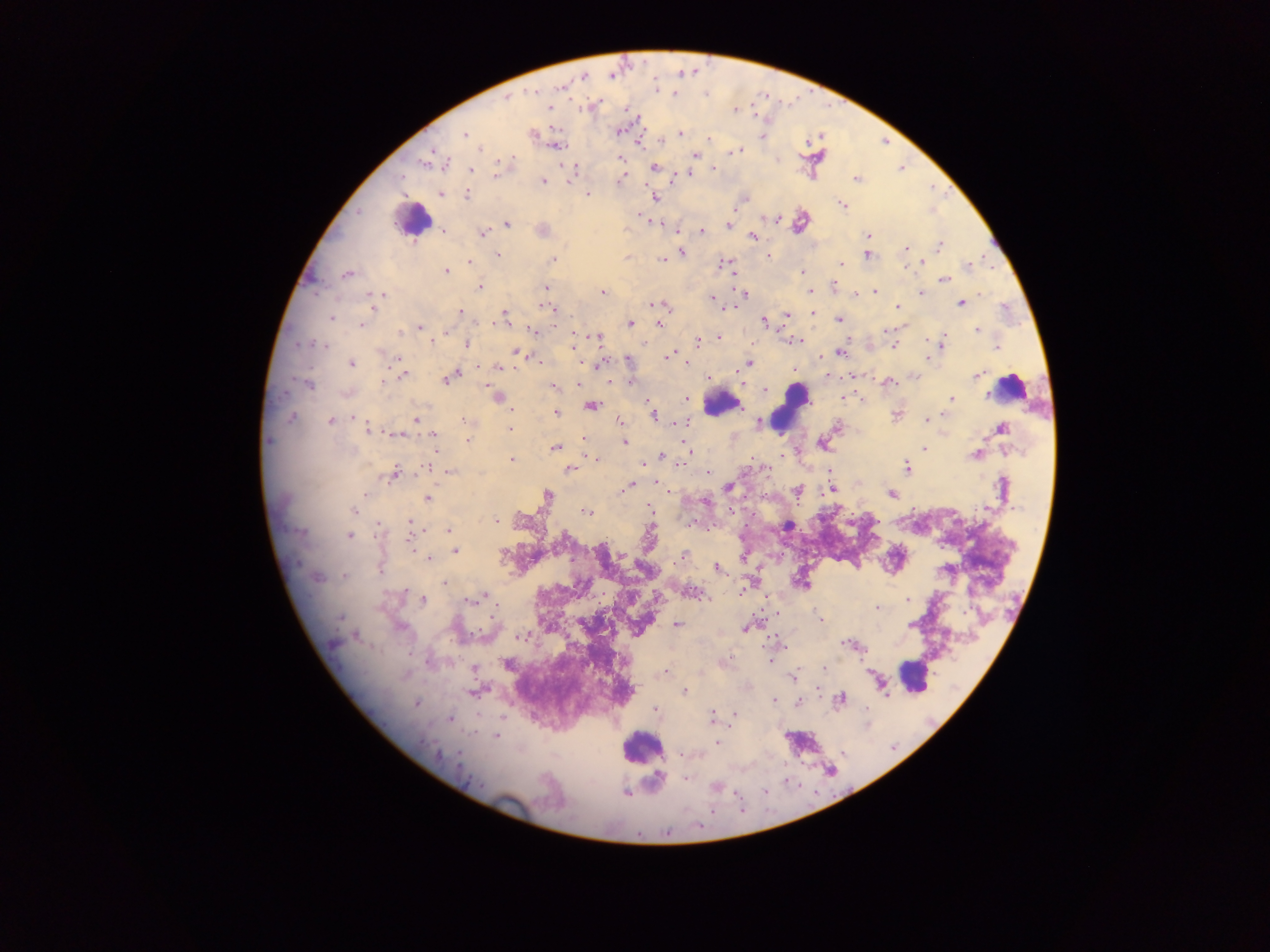
Approximate centers as x y in pixels.
Summary:
  - Plasmodium parasite locations: 561 87; 533 93; 507 98; 548 108; 735 110; 618 131; 680 133; 465 135; 532 135; 763 136; 709 139; 556 145; 479 148; 739 149; 694 155; 621 158; 425 162; 445 164; 655 167; 713 168; 471 169; 573 170; 497 173; 688 174; 857 179; 619 180; 543 181; 441 194; 588 194; 467 195; 655 197; 744 199; 842 204; 508 224; 728 224; 542 230; 702 230; 444 231; 482 233; 869 236; 753 237; 940 246; 906 248; 682 252; 498 255; 868 255; 768 256; 661 259; 553 260; 470 262; 725 263; 923 263; 841 264; 967 266; 803 271; 446 272; 347 275; 943 279; 479 286; 834 287; 546 288; 810 291; 876 291; 603 292; 920 292; 382 294; 743 294; 857 295; 370 296; 712 300; 372 301; 961 303; 658 304; 897 306; 549 308; 461 311; 504 313; 812 313; 787 315; 331 318; 839 319; 504 321; 764 322; 630 323; 361 324; 658 324; 420 327; 978 330; 533 331; 886 331; 400 332; 596 338; 718 338; 431 341; 698 341; 797 341; 941 343; 311 344; 467 344; 324 346; 892 346; 997 348; 518 353; 840 353; 668 356; 927 358; 399 360; 628 360; 685 362; 748 363; 351 364; 497 367; 454 374; 402 375; 827 375; 977 376; 450 378; 385 381; 631 382; 888 382; 307 383; 577 383; 554 388; 766 390; 495 396; 686 397; 844 398; 952 398; 592 406; 555 413; 895 414; 654 415; 291 418; 354 418; 415 420; 462 420; 620 420; 926 420; 330 421; 683 423; 758 424; 369 429; 1001 429; 510 430; 397 434; 433 435; 583 439; 468 440; 268 441; 624 442; 822 444; 555 448; 924 448; 689 452; 661 455; 974 455; 594 459; 511 460; 643 463; 429 467; 906 468; 570 470; 450 472; 393 474; 708 474; 657 482; 628 487; 728 487; 797 490; 832 490; 364 495; 548 495; 892 495; 428 498; 353 510; 586 513; 496 521; 409 523; 789 526; 378 527; 448 530; 350 536; 410 541; 455 550; 684 555; 429 558; 718 569; 380 571; 343 576; 318 578; 443 583; 691 592; 486 597; 479 598; 423 600; 908 600; 470 601; 877 608; 341 618; 820 619; 677 624; 910 625; 401 627; 747 627; 521 635; 355 636; 850 645; 508 664; 475 668; 823 669; 665 673; 792 677; 884 690; 473 691; 685 691; 840 699; 773 700; 416 703; 799 703; 655 710; 735 715; 711 716; 450 718; 497 735; 716 743; 459 754; 474 782; 715 787; 625 793
  - Leukocyte locations: 413 220; 1010 388; 722 403; 793 406; 913 676; 641 747
  - Field of view: single
  - Country: Ghana
  - Capture: mobile-phone photograph through a microscope
  - Image size: 1270×952 pixels
  - Preparation: thick blood film